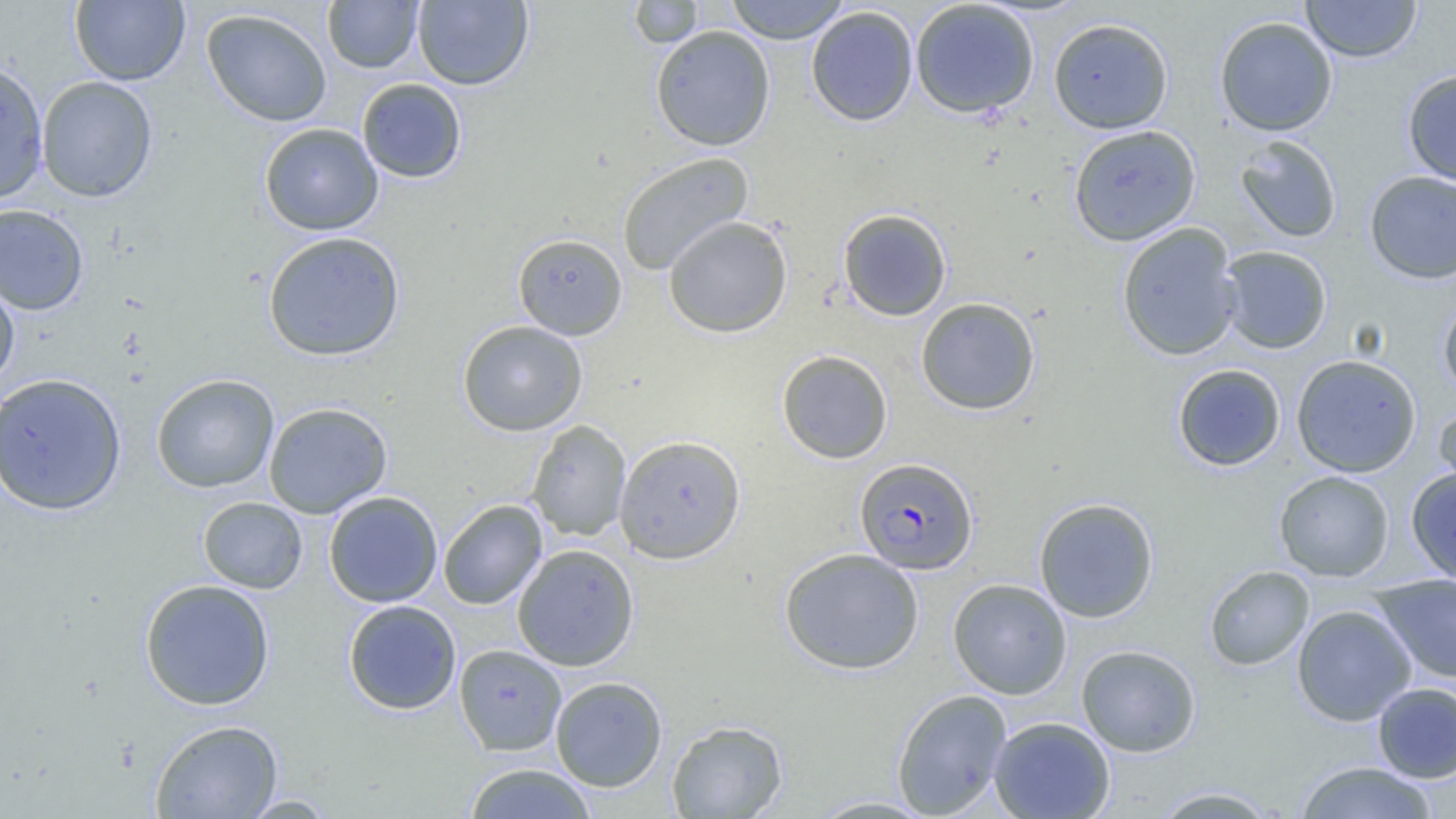
Summary:
  - Coordinate format: approximate bounding boxes as (x1,y1)-(x2,y2) corner pairs in pixels
  - Uninfected red blood cell locations: (70,0)-(190,86), (322,0)-(425,74), (628,0)-(704,48), (725,0)-(851,44), (1301,0)-(1421,62), (413,1)-(534,89), (909,1)-(1040,118), (806,6)-(918,126), (201,8)-(333,127), (1214,16)-(1338,137), (1048,17)-(1174,134), (651,25)-(775,151), (0,59)-(50,204), (1402,69)-(1456,187), (36,76)-(158,202), (356,78)-(467,183), (259,122)-(384,236), (1067,124)-(1201,246), (1235,135)-(1342,243), (616,152)-(754,275), (1364,170)-(1456,284), (0,204)-(89,315), (838,208)-(952,321), (663,215)-(793,338), (1116,223)-(1242,361), (263,231)-(405,361), (512,233)-(627,340), (1217,245)-(1333,354), (0,268)-(20,391), (1438,296)-(1456,399), (915,297)-(1041,415), (457,320)-(588,436), (776,349)-(893,464), (1291,354)-(1422,477), (1172,364)-(1286,471), (0,372)-(127,516), (151,373)-(279,493), (263,401)-(392,519), (1433,405)-(1456,504), (526,420)-(632,541), (613,434)-(746,565), (1406,466)-(1456,585), (1274,470)-(1395,582), (323,490)-(443,608), (197,496)-(308,594), (1033,497)-(1159,623), (438,500)-(547,610), (512,543)-(640,671), (778,548)-(924,675), (1203,565)-(1315,671), (1371,573)-(1456,684), (948,578)-(1072,699), (139,579)-(276,711), (342,599)-(462,715), (1291,604)-(1417,726), (454,644)-(567,756), (1076,644)-(1201,757), (549,676)-(668,792), (1372,682)-(1456,783), (892,688)-(1012,818), (989,716)-(1115,819), (149,719)-(283,819), (666,719)-(788,818), (1294,761)-(1439,818), (462,763)-(598,818), (1149,786)-(1283,818), (237,794)-(340,817), (806,795)-(939,818)
  - Plasmodium falciparum-infected red blood cell locations: (854,457)-(978,574)
  - Slide-level diagnosis: Plasmodium falciparum
  - Field of view: single
  - Modality: optical microscopy
  - Image size: 1456×819 pixels
  - Magnification: 1000x
  - Preparation: thin blood smear